Assess this cell for malaria.
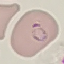

It is parasitized.

capture = smartphone through the microscope eyepiece
image type = cell patch, automatically extracted from a larger field of view and resized to 64 × 64 pixels
preparation = thin blood film
stain = Giemsa